Assess this cell for malaria.
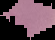

Parasitized.

From a thin blood smear. Image is 55×40 pixels. Segmented cell region on a black background.